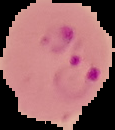

Result: malaria parasites detected. From a thin blood smear. Cell region segmented out of the field of view; the surrounding area is masked to black. Image is 115×130 pixels.